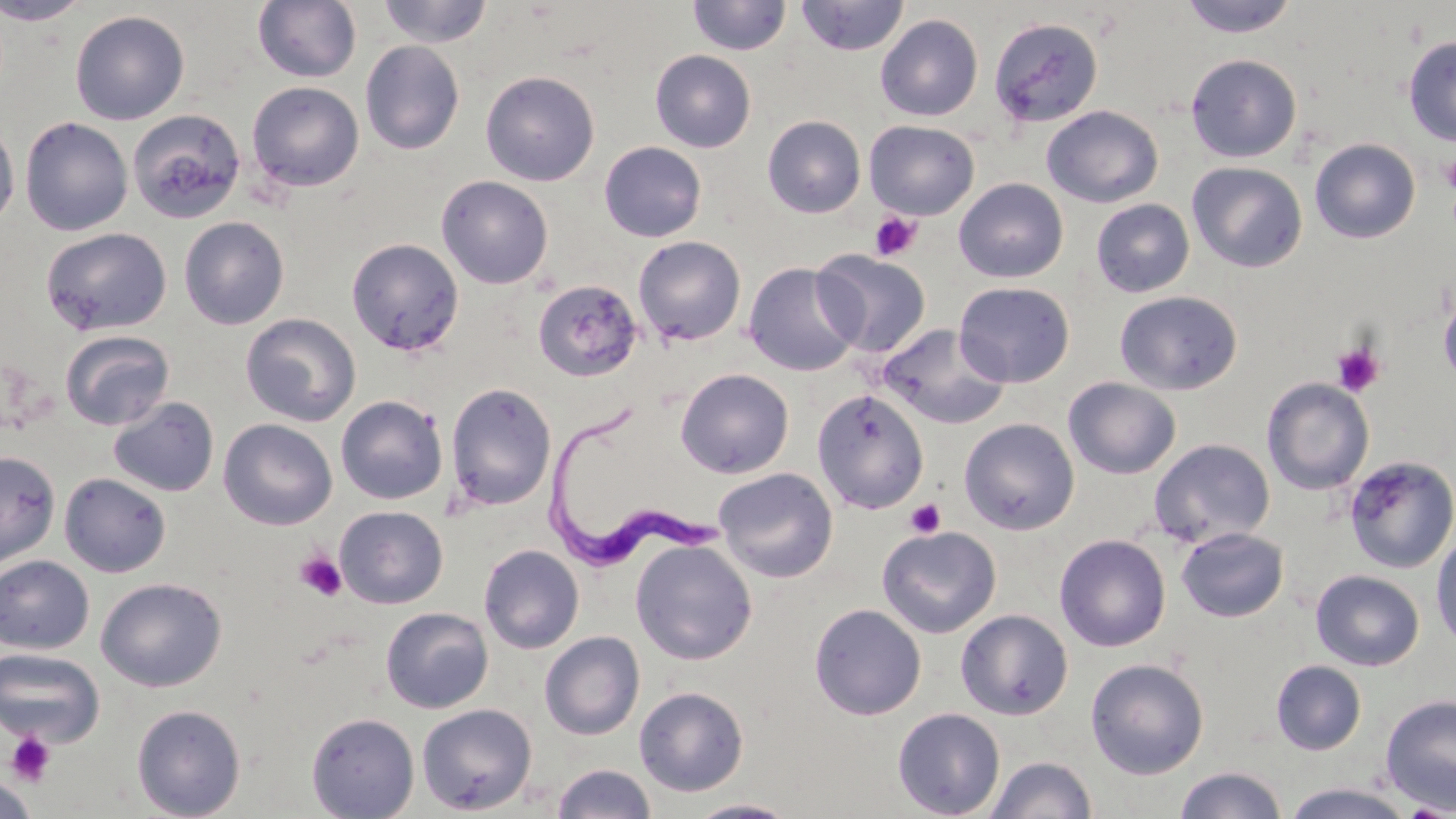

slide-level diagnosis = Trypanosoma brucei
stain = May-Grünwald-Giemsa
modality = light microscopy
preparation = thin blood smear
Trypanosoma brucei locations = approximate bounding boxes as named x1/y1/x2/y2 corners in pixels: (x1=544, y1=395, x2=725, y2=572)
platelet locations = approximate bounding boxes as named x1/y1/x2/y2 corners in pixels: (x1=1440, y1=154, x2=1456, y2=191), (x1=869, y1=212, x2=922, y2=262), (x1=1331, y1=342, x2=1386, y2=398), (x1=905, y1=498, x2=946, y2=538), (x1=294, y1=551, x2=347, y2=601), (x1=5, y1=731, x2=56, y2=786)
image size = 1456×819 pixels
field of view = one of a larger specimen
uninfected red blood cell locations = approximate bounding boxes as named x1/y1/x2/y2 corners in pixels: (x1=0, y1=0, x2=92, y2=26), (x1=252, y1=0, x2=362, y2=83), (x1=377, y1=0, x2=492, y2=48), (x1=687, y1=0, x2=791, y2=56), (x1=795, y1=0, x2=909, y2=56), (x1=1177, y1=0, x2=1300, y2=38), (x1=70, y1=10, x2=190, y2=125), (x1=875, y1=14, x2=984, y2=121), (x1=988, y1=17, x2=1104, y2=130), (x1=1402, y1=34, x2=1456, y2=146), (x1=360, y1=40, x2=465, y2=155), (x1=650, y1=49, x2=756, y2=153), (x1=1185, y1=53, x2=1302, y2=162), (x1=480, y1=70, x2=600, y2=186), (x1=247, y1=81, x2=364, y2=193), (x1=1042, y1=105, x2=1163, y2=208), (x1=126, y1=108, x2=246, y2=224), (x1=762, y1=115, x2=866, y2=218), (x1=20, y1=116, x2=133, y2=236), (x1=0, y1=117, x2=20, y2=231), (x1=864, y1=120, x2=980, y2=219), (x1=1309, y1=138, x2=1421, y2=244), (x1=599, y1=141, x2=707, y2=242), (x1=1187, y1=161, x2=1308, y2=273), (x1=436, y1=175, x2=554, y2=290), (x1=954, y1=178, x2=1068, y2=283), (x1=1090, y1=198, x2=1195, y2=298), (x1=178, y1=216, x2=290, y2=329), (x1=41, y1=226, x2=172, y2=336), (x1=633, y1=235, x2=746, y2=346), (x1=346, y1=237, x2=465, y2=355), (x1=813, y1=249, x2=932, y2=357), (x1=743, y1=262, x2=862, y2=376), (x1=1438, y1=278, x2=1456, y2=389), (x1=533, y1=279, x2=643, y2=382), (x1=954, y1=281, x2=1075, y2=387), (x1=1114, y1=290, x2=1243, y2=396), (x1=241, y1=313, x2=361, y2=427), (x1=876, y1=323, x2=1012, y2=431), (x1=60, y1=330, x2=175, y2=431), (x1=675, y1=368, x2=794, y2=479), (x1=1063, y1=377, x2=1181, y2=479), (x1=1261, y1=377, x2=1375, y2=495), (x1=445, y1=383, x2=557, y2=511), (x1=811, y1=388, x2=930, y2=514), (x1=336, y1=395, x2=448, y2=505), (x1=108, y1=396, x2=219, y2=497), (x1=218, y1=418, x2=338, y2=530), (x1=959, y1=418, x2=1080, y2=535), (x1=1149, y1=438, x2=1275, y2=548), (x1=0, y1=450, x2=60, y2=569), (x1=1343, y1=456, x2=1456, y2=574), (x1=713, y1=467, x2=839, y2=582), (x1=59, y1=472, x2=171, y2=577), (x1=335, y1=505, x2=448, y2=609), (x1=877, y1=525, x2=1001, y2=638), (x1=1176, y1=526, x2=1289, y2=622), (x1=1430, y1=530, x2=1456, y2=650), (x1=1054, y1=534, x2=1171, y2=652), (x1=630, y1=539, x2=758, y2=665), (x1=479, y1=544, x2=584, y2=654), (x1=0, y1=554, x2=95, y2=654), (x1=1311, y1=570, x2=1425, y2=671), (x1=96, y1=577, x2=227, y2=692), (x1=809, y1=603, x2=926, y2=720), (x1=380, y1=607, x2=493, y2=714), (x1=955, y1=609, x2=1073, y2=720), (x1=539, y1=631, x2=644, y2=741), (x1=0, y1=648, x2=105, y2=748), (x1=1085, y1=658, x2=1209, y2=779), (x1=1271, y1=660, x2=1367, y2=755), (x1=633, y1=686, x2=749, y2=796), (x1=1380, y1=693, x2=1456, y2=814), (x1=131, y1=703, x2=246, y2=819), (x1=417, y1=703, x2=537, y2=814), (x1=892, y1=707, x2=1006, y2=819), (x1=306, y1=711, x2=419, y2=818), (x1=986, y1=756, x2=1097, y2=818), (x1=551, y1=763, x2=657, y2=819), (x1=1174, y1=765, x2=1288, y2=819), (x1=0, y1=774, x2=39, y2=818), (x1=1281, y1=782, x2=1417, y2=818), (x1=683, y1=798, x2=800, y2=818)
magnification = 1000x